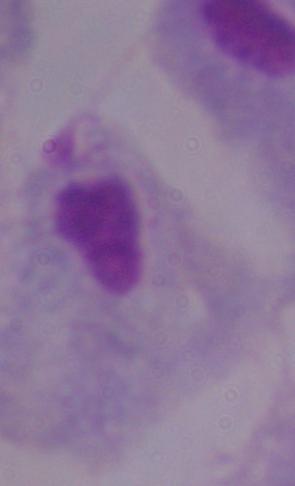
modality = micrograph
magnification = 1000x
identification = trichomonad